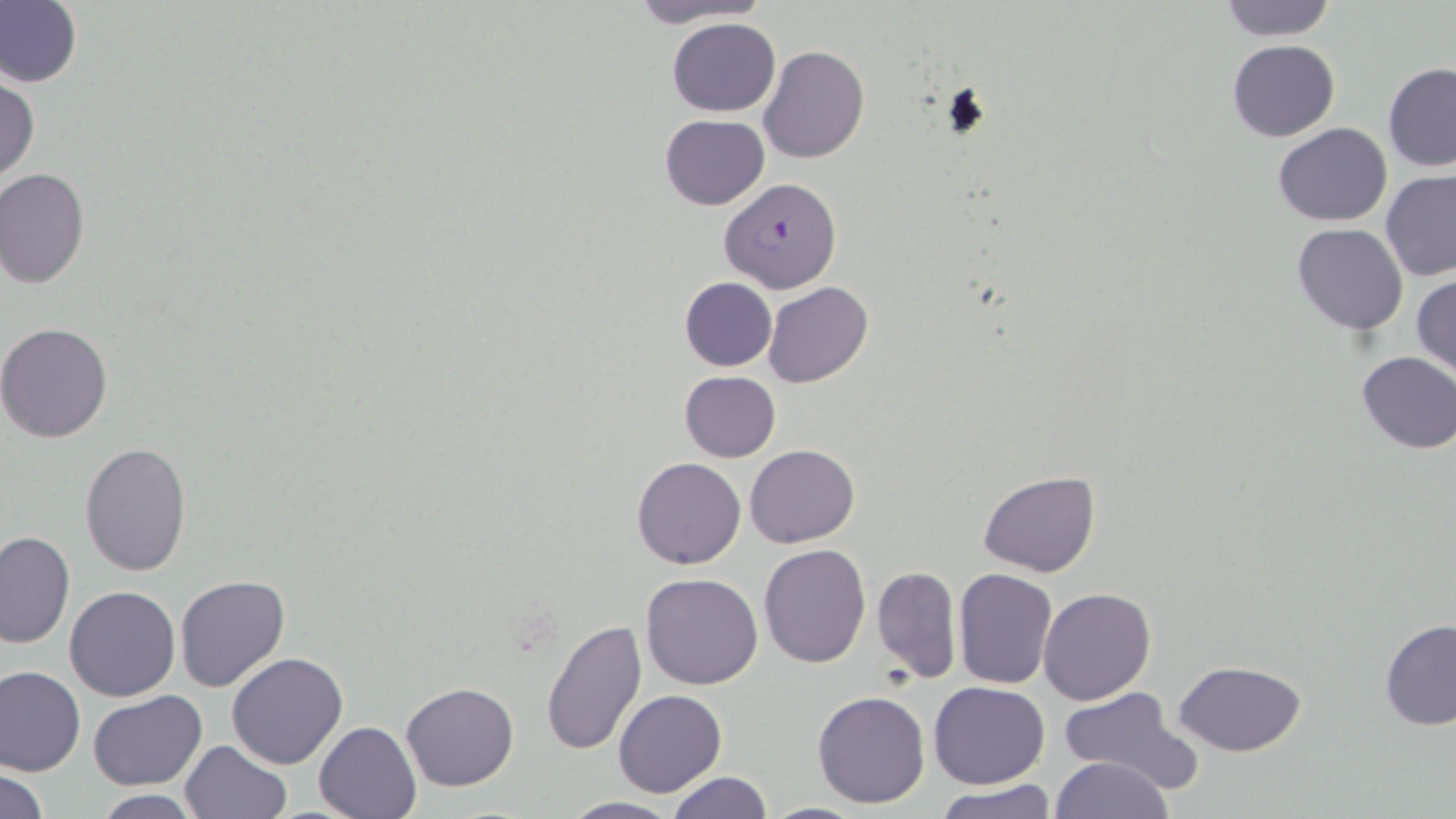
Summary:
  - Coordinate format: approximate bounding boxes as named x1/y1/x2/y2 corners in pixels
  - Uninfected red blood cell locations: (x1=0, y1=0, x2=82, y2=89), (x1=622, y1=0, x2=776, y2=28), (x1=1215, y1=0, x2=1338, y2=41), (x1=667, y1=16, x2=781, y2=117), (x1=1227, y1=39, x2=1340, y2=141), (x1=757, y1=45, x2=870, y2=164), (x1=1383, y1=65, x2=1455, y2=170), (x1=1, y1=75, x2=39, y2=183), (x1=659, y1=115, x2=769, y2=211), (x1=1273, y1=122, x2=1391, y2=227), (x1=0, y1=169, x2=89, y2=289), (x1=1381, y1=169, x2=1456, y2=282), (x1=1292, y1=223, x2=1408, y2=334), (x1=1411, y1=273, x2=1456, y2=380), (x1=678, y1=277, x2=777, y2=371), (x1=761, y1=282, x2=874, y2=388), (x1=0, y1=321, x2=116, y2=442), (x1=1354, y1=351, x2=1456, y2=454), (x1=679, y1=371, x2=781, y2=461), (x1=79, y1=441, x2=192, y2=576), (x1=745, y1=445, x2=859, y2=547), (x1=630, y1=458, x2=745, y2=571), (x1=978, y1=470, x2=1100, y2=578), (x1=0, y1=530, x2=74, y2=649), (x1=758, y1=544, x2=870, y2=666), (x1=873, y1=566, x2=961, y2=684), (x1=952, y1=567, x2=1057, y2=690), (x1=641, y1=573, x2=764, y2=690), (x1=174, y1=575, x2=289, y2=692), (x1=64, y1=585, x2=180, y2=701), (x1=1039, y1=587, x2=1155, y2=705), (x1=1379, y1=618, x2=1456, y2=730), (x1=539, y1=619, x2=648, y2=757), (x1=226, y1=652, x2=347, y2=769), (x1=1174, y1=660, x2=1308, y2=756), (x1=0, y1=665, x2=86, y2=777), (x1=928, y1=681, x2=1050, y2=788), (x1=400, y1=682, x2=520, y2=792), (x1=1058, y1=688, x2=1194, y2=790), (x1=614, y1=689, x2=726, y2=795), (x1=88, y1=690, x2=207, y2=790), (x1=812, y1=691, x2=929, y2=809), (x1=315, y1=720, x2=422, y2=818), (x1=179, y1=739, x2=291, y2=819), (x1=1050, y1=755, x2=1175, y2=819), (x1=0, y1=766, x2=49, y2=818), (x1=666, y1=773, x2=774, y2=819), (x1=936, y1=782, x2=1056, y2=819), (x1=90, y1=791, x2=204, y2=818), (x1=556, y1=795, x2=684, y2=817), (x1=750, y1=801, x2=879, y2=819)
  - Plasmodium falciparum-infected red blood cell locations: (x1=719, y1=177, x2=841, y2=293)
  - Slide-level diagnosis: Plasmodium falciparum
  - Magnification: 1000x
  - Modality: light microscopy
  - Field of view: single
  - Image size: 1456×819 pixels
  - Stain: May-Grünwald-Giemsa
  - Preparation: thin blood film